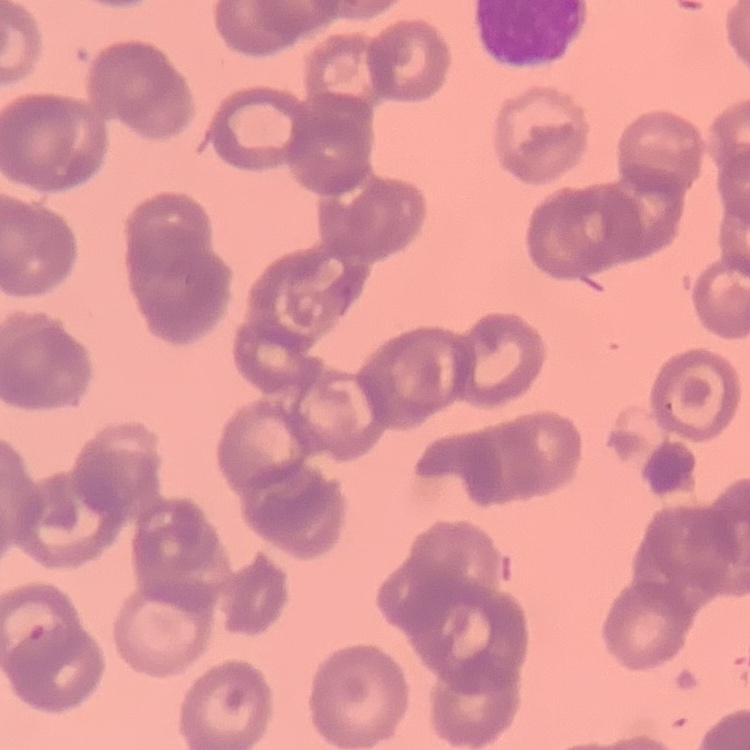
The erythrocytes show rouleaux formation. Square crop of a larger photomicrograph. Stained with either Field's or Giemsa. Thin blood film.